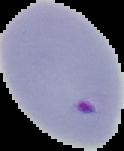
Summary:
  - Image size: 124×151 pixels
  - Preparation: thin blood smear
  - Image type: segmented cell region on a black background
  - Malaria status: parasitized